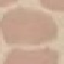
{
  "malaria_status": "uninfected",
  "capture": "smartphone camera at the microscope eyepiece",
  "preparation": "thin blood smear",
  "stain": "Giemsa",
  "image_type": "cell patch, automatically extracted from a larger field of view and resized to 64 × 64 pixels"
}